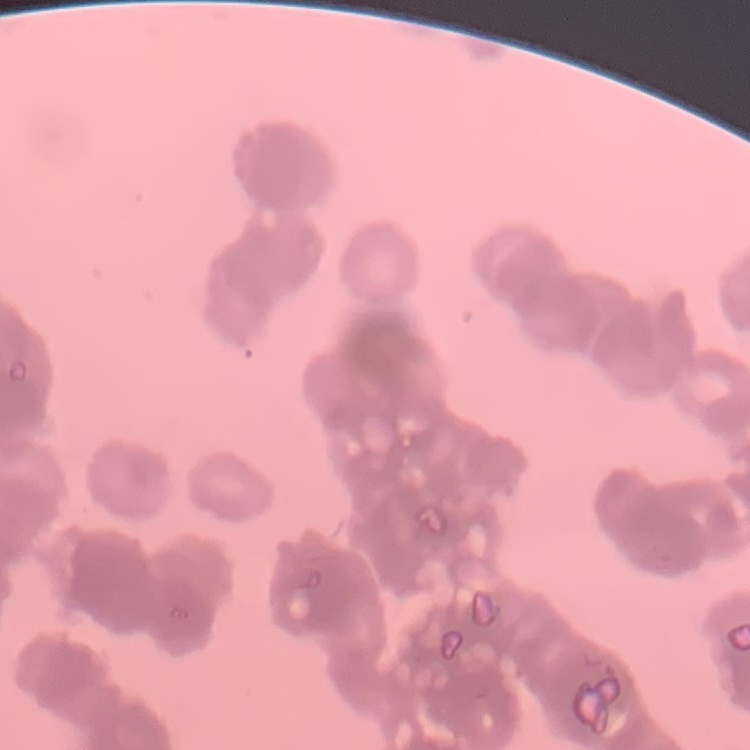
Summary:
  - Erythrocyte morphology: rouleaux formation
  - Preparation: thin blood film
  - Stain: Field's or Giemsa
  - Image type: one tile cut from a larger photomicrograph